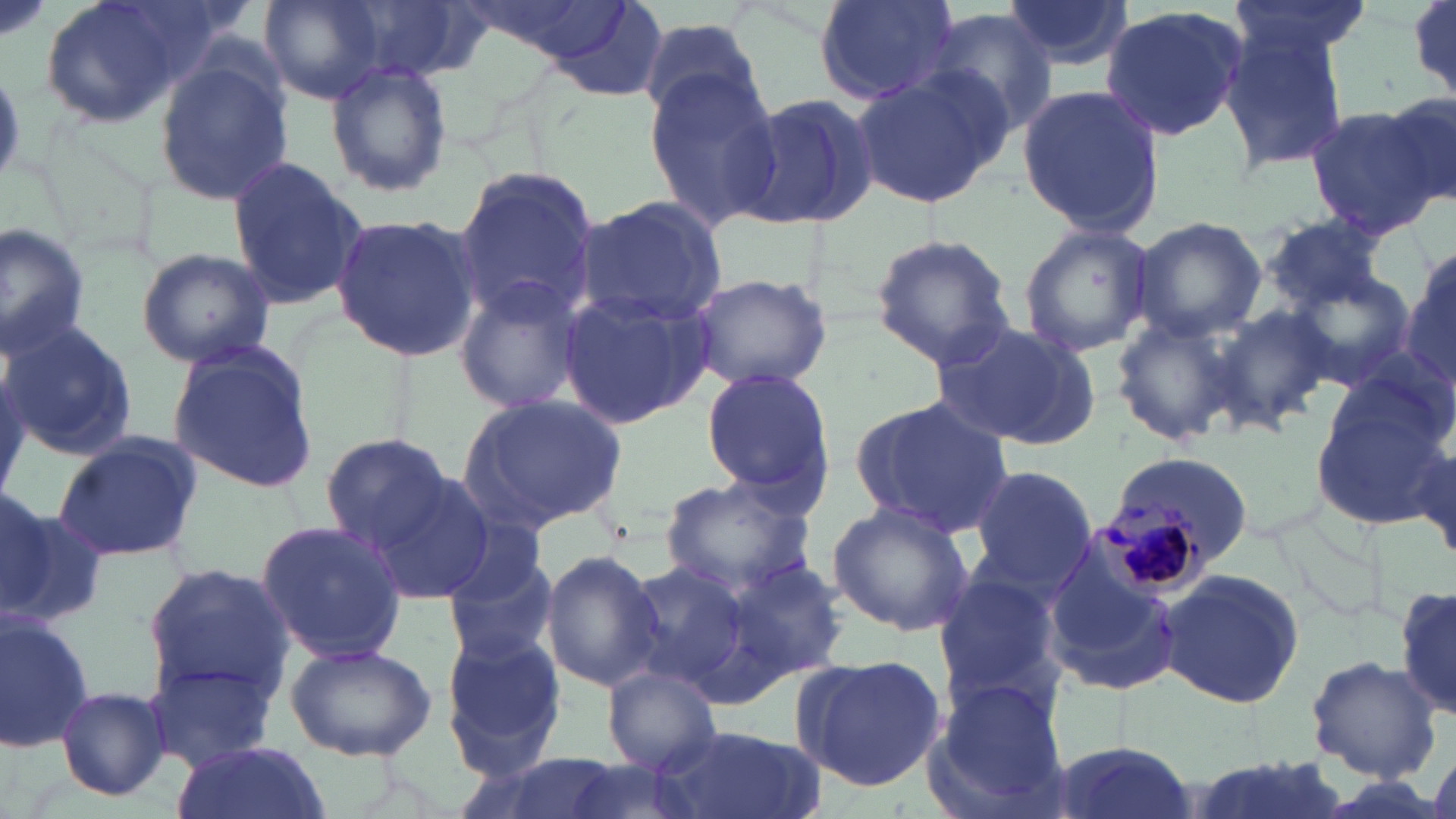

slide_level_diagnosis: Plasmodium malariae
magnification: 1000x
plasmodium_malariae_infected_red_blood_cell_locations: 'approximate bounding boxes as [x1, y1, x2, y2] in pixels: [1099, 494, 1209, 595]'
stain: May-Grünwald-Giemsa
preparation: thin blood film
image_size: 1456×819 pixels
modality: optical microscopy
uninfected_red_blood_cell_locations: 'approximate bounding boxes as [x1, y1, x2, y2] in pixels: [38, 0, 206, 130], [260, 0, 391, 104], [347, 0, 493, 83], [446, 0, 629, 66], [812, 0, 959, 105], [1002, 0, 1136, 73], [1227, 0, 1371, 67], [1410, 0, 1455, 95], [535, 2, 672, 100], [1097, 6, 1249, 141], [928, 8, 1062, 137], [640, 14, 765, 124], [1220, 24, 1350, 178], [152, 55, 293, 206], [325, 59, 453, 198], [643, 70, 781, 226], [852, 70, 1006, 209], [1017, 85, 1166, 240], [1376, 90, 1455, 213], [730, 91, 879, 233], [1304, 106, 1443, 238], [223, 157, 369, 310], [454, 164, 603, 325], [573, 196, 728, 326], [1263, 212, 1391, 312], [329, 213, 482, 361], [1129, 216, 1267, 340], [0, 222, 95, 359], [1018, 223, 1155, 357], [869, 232, 1018, 372], [1402, 242, 1456, 399], [136, 247, 276, 368], [1275, 262, 1417, 393], [685, 271, 833, 392], [452, 277, 587, 417], [559, 286, 715, 429], [1211, 305, 1333, 433], [1113, 310, 1250, 448], [930, 319, 1105, 450], [2, 320, 138, 458], [166, 340, 321, 493], [700, 366, 837, 511], [1309, 370, 1452, 532], [456, 394, 628, 535], [852, 396, 1016, 539], [320, 433, 457, 552], [51, 434, 202, 564], [1411, 434, 1455, 564], [963, 464, 1099, 600], [362, 471, 497, 604], [660, 476, 818, 596], [0, 493, 98, 631], [827, 499, 972, 637], [1265, 506, 1388, 622], [252, 519, 407, 664], [1040, 543, 1181, 699], [441, 546, 560, 667], [542, 551, 663, 692], [619, 558, 755, 699], [728, 561, 850, 680], [142, 564, 296, 704], [1155, 568, 1307, 708], [933, 572, 1066, 713], [1396, 579, 1455, 722], [0, 610, 96, 756], [438, 632, 567, 772], [282, 640, 438, 762], [791, 655, 947, 792], [1307, 656, 1440, 780], [146, 658, 279, 771], [602, 664, 724, 778], [930, 675, 1070, 811], [54, 686, 171, 803], [654, 725, 817, 819], [1043, 739, 1197, 819], [171, 742, 330, 819], [452, 752, 644, 819], [1183, 754, 1357, 819], [559, 758, 707, 819]'
field_of_view: single